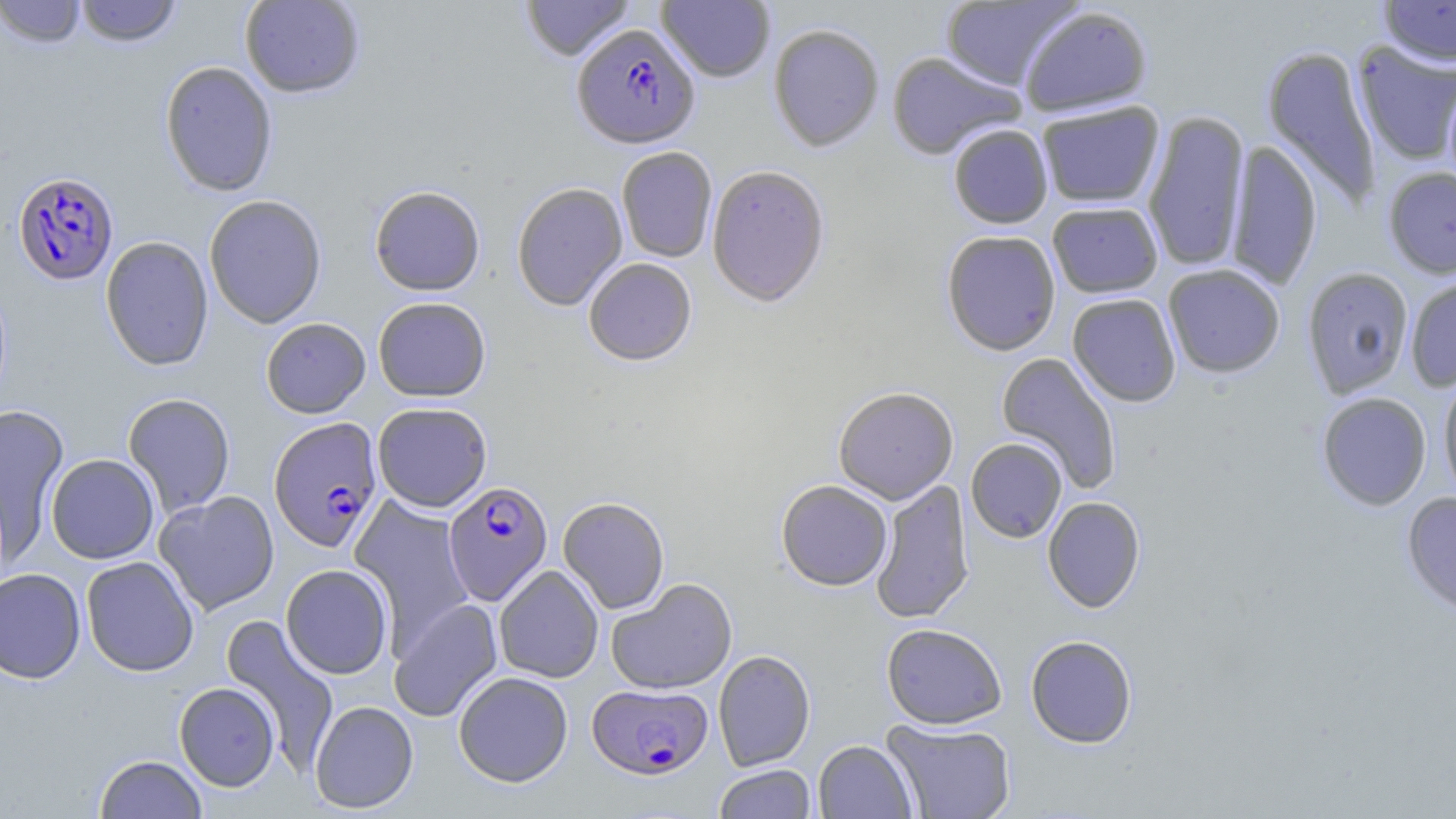
{
  "slide_level_diagnosis": "Plasmodium falciparum",
  "preparation": "thin blood film",
  "image_size": "1456×819 pixels",
  "magnification": "1000x",
  "uninfected_red_blood_cell_locations": "approximate bounding boxes as (x1, y1, x2, y2) in pixels: (0, 0, 86, 48), (74, 0, 182, 48), (240, 0, 365, 99), (521, 0, 635, 62), (657, 0, 775, 83), (1379, 0, 1456, 67), (940, 1, 1081, 89), (1019, 6, 1153, 117), (768, 24, 884, 153), (1352, 41, 1456, 166), (1261, 44, 1383, 210), (886, 52, 1025, 160), (159, 61, 278, 197), (1443, 74, 1456, 201), (1036, 101, 1165, 209), (1142, 110, 1250, 273), (948, 125, 1053, 229), (1225, 139, 1323, 290), (617, 148, 717, 263), (707, 165, 831, 308), (1383, 167, 1456, 279), (512, 183, 628, 312), (370, 187, 485, 297), (204, 195, 327, 329), (1047, 202, 1163, 298), (941, 231, 1061, 356), (100, 236, 214, 371), (583, 258, 697, 366), (1162, 264, 1285, 378), (1302, 267, 1414, 398), (1405, 275, 1456, 392), (1067, 293, 1182, 407), (373, 297, 491, 402), (261, 318, 371, 418), (996, 351, 1123, 494), (1438, 374, 1456, 507), (833, 387, 958, 504), (1316, 392, 1431, 510), (122, 393, 236, 517), (372, 402, 492, 512), (0, 403, 69, 553), (966, 438, 1067, 543), (46, 454, 159, 564), (871, 478, 975, 625), (776, 480, 892, 592), (154, 491, 279, 615), (1402, 492, 1456, 616), (557, 496, 670, 614), (1042, 496, 1146, 613), (349, 497, 474, 646), (81, 557, 199, 677), (280, 564, 393, 679), (494, 565, 604, 683), (0, 568, 85, 683), (606, 578, 738, 695), (389, 598, 503, 722), (221, 615, 339, 771), (881, 623, 1007, 729), (1025, 635, 1138, 748), (713, 650, 815, 771), (454, 671, 573, 787), (174, 682, 280, 791), (309, 700, 419, 813), (882, 718, 1016, 819), (813, 740, 917, 818), (94, 754, 208, 818), (714, 764, 816, 818)",
  "field_of_view": "one of a larger specimen",
  "modality": "optical microscopy",
  "stain": "May-Grünwald-Giemsa",
  "plasmodium_falciparum_infected_red_blood_cell_locations": "approximate bounding boxes as (x1, y1, x2, y2) in pixels: (572, 25, 700, 152), (12, 172, 118, 285), (269, 417, 384, 552), (443, 481, 553, 605), (587, 683, 713, 780)"
}